Name the parasite shown.
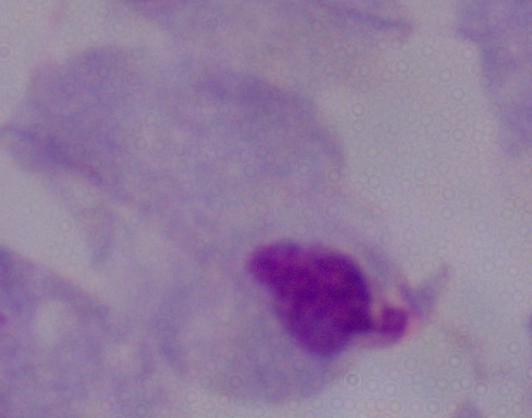
A trichomonad.

modality = micrograph
magnification = 1000x